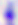
identification = Toxoplasma gondii
magnification = 400x
modality = photomicrograph